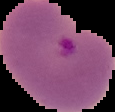

result = Plasmodium parasites identified
image type = segmented cell region with the area outside set to black
image size = 115×112 pixels
preparation = thin blood film